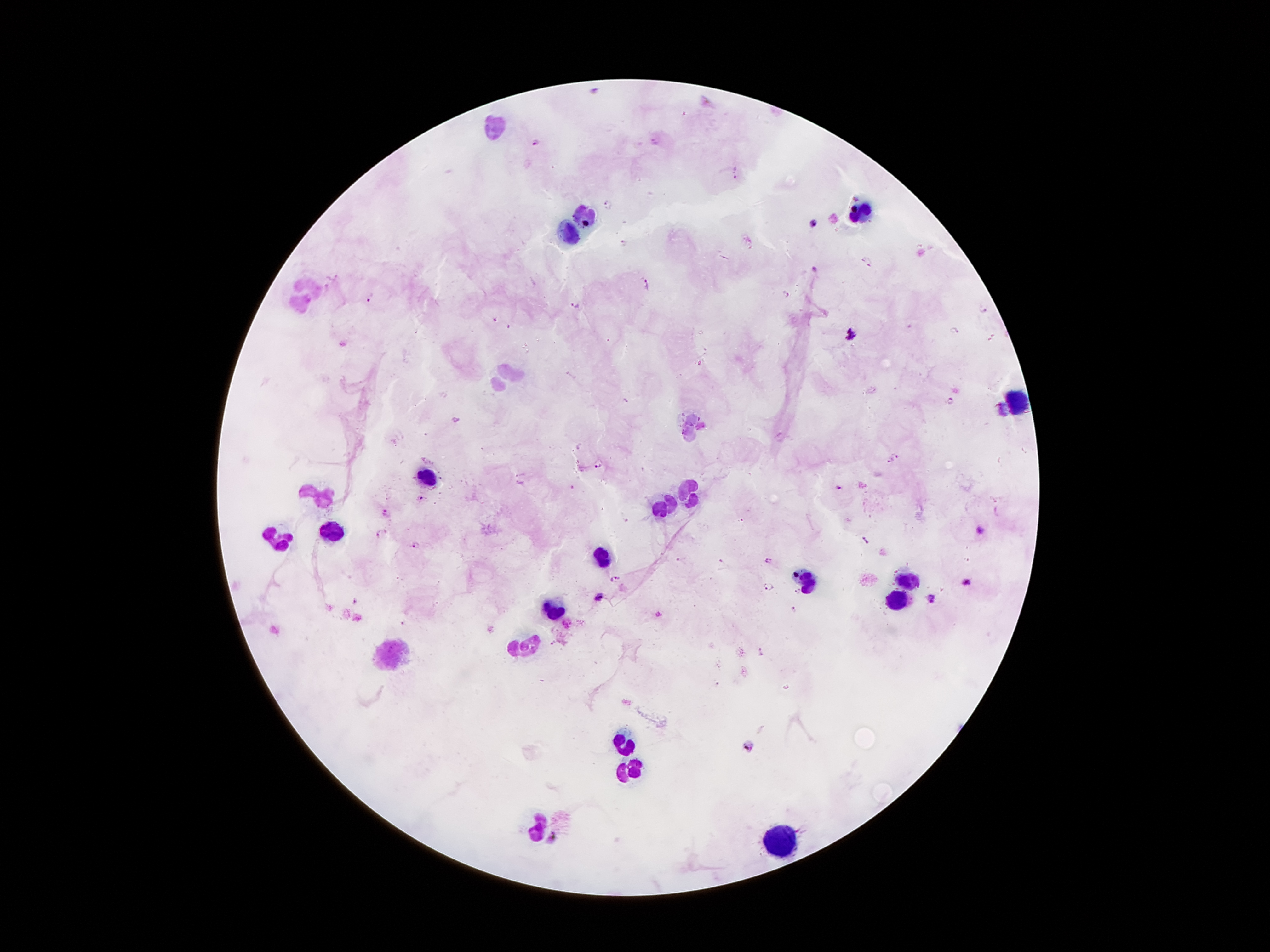
coordinate format = approximate centers as {x, y} in pixels
malaria parasite locations = {656, 141}, {536, 142}, {735, 173}, {609, 204}, {814, 225}, {625, 244}, {867, 262}, {816, 271}, {647, 284}, {785, 294}, {370, 297}, {577, 305}, {983, 309}, {495, 319}, {956, 331}, {852, 336}, {626, 400}, {950, 400}, {1003, 409}, {456, 420}, {895, 457}, {886, 461}, {600, 464}, {838, 488}, {420, 497}, {386, 513}, {981, 530}, {381, 532}, {866, 541}, {415, 545}, {680, 559}, {768, 560}, {721, 561}, {614, 579}, {965, 581}, {767, 586}, {798, 591}, {599, 597}, {930, 600}, {354, 602}, {794, 608}, {658, 613}, {402, 624}, {552, 641}, {761, 652}, {716, 685}, {749, 746}, {551, 837}
leukocyte locations = {494, 125}, {587, 212}, {859, 212}, {566, 234}, {302, 292}, {505, 382}, {1015, 404}, {693, 429}, {427, 472}, {689, 492}, {320, 496}, {667, 505}, {277, 531}, {333, 533}, {605, 558}, {808, 574}, {902, 580}, {894, 597}, {554, 607}, {521, 646}, {398, 654}, {624, 742}, {630, 769}, {536, 818}, {784, 843}
patient malaria status = positive for Plasmodium falciparum
stain = Giemsa
field of view = single
capture = smartphone camera through the microscope eyepiece
magnification = 100x
preparation = thick blood film
image size = 1270×952 pixels